Comment on the morphology of the red blood cells.
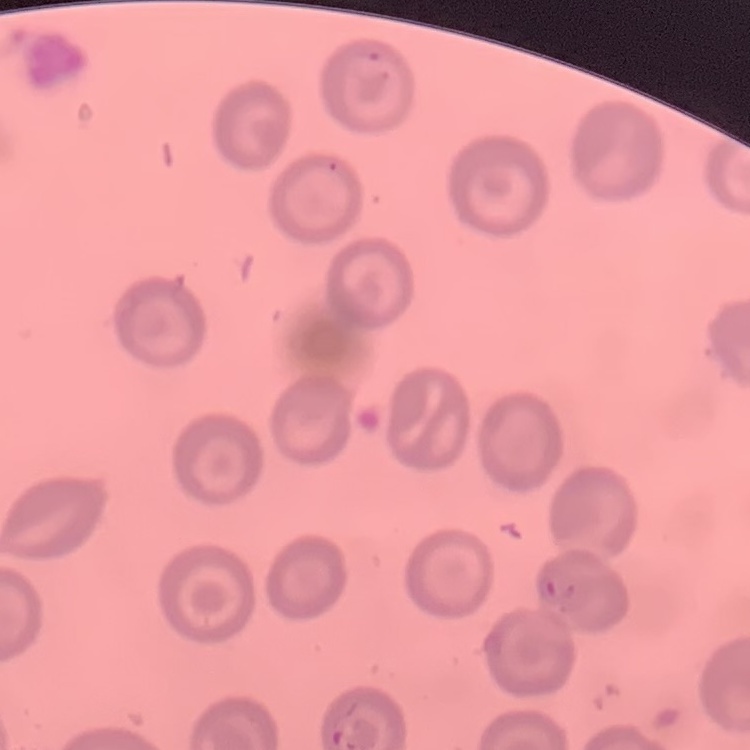

They show no rouleaux formation.

Summary:
  - Stain: Field's or Giemsa
  - Preparation: thin blood smear
  - Image type: square crop of a larger photomicrograph